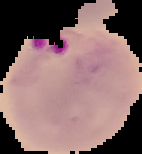
image_size: 142×154 pixels
image_type: segmented cell region with the area outside set to black
result: Plasmodium parasites detected
preparation: thin blood smear